Classify this cell by malaria status.
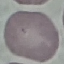
Uninfected.

Summary:
  - Image type: cell patch, automatically extracted from a larger field of view and resized to 64 × 64 pixels
  - Preparation: thin blood smear
  - Capture: smartphone camera at the microscope eyepiece
  - Stain: Giemsa